Give the extent of all uninfected red blood cells.
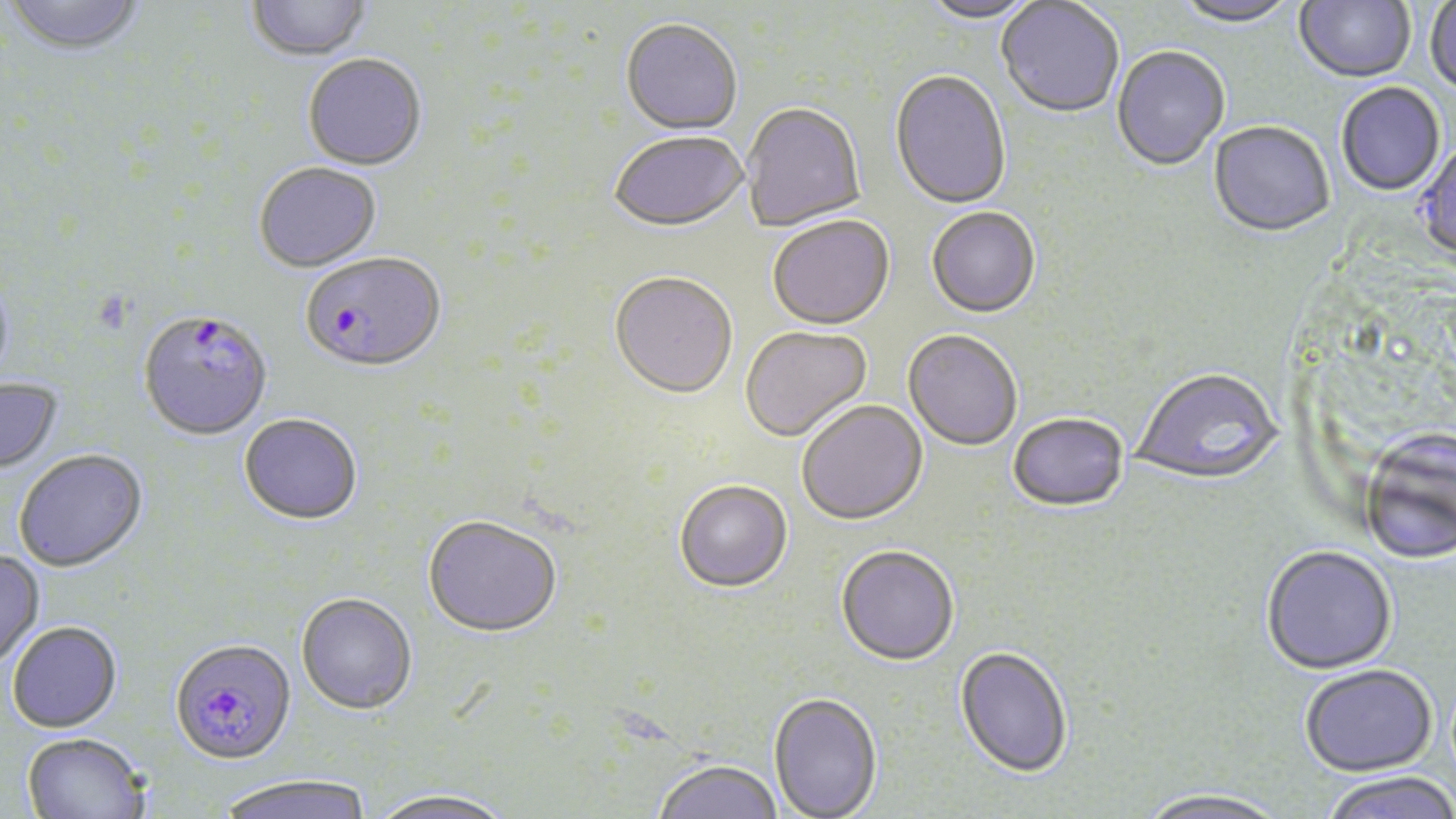

Approximate bounding boxes as named x1/y1/x2/y2 corners in pixels.
Uninfected red blood cells: (x1=4, y1=0, x2=147, y2=59), (x1=920, y1=0, x2=1041, y2=27), (x1=1294, y1=0, x2=1416, y2=85), (x1=245, y1=1, x2=374, y2=64), (x1=996, y1=1, x2=1124, y2=120), (x1=1172, y1=1, x2=1299, y2=29), (x1=1425, y1=1, x2=1456, y2=97), (x1=620, y1=21, x2=742, y2=137), (x1=1112, y1=47, x2=1230, y2=173), (x1=303, y1=56, x2=427, y2=173), (x1=889, y1=72, x2=1011, y2=211), (x1=1336, y1=84, x2=1445, y2=197), (x1=741, y1=105, x2=866, y2=232), (x1=1208, y1=123, x2=1335, y2=239), (x1=610, y1=134, x2=748, y2=234), (x1=1414, y1=142, x2=1456, y2=264), (x1=254, y1=164, x2=382, y2=274), (x1=926, y1=209, x2=1041, y2=321), (x1=768, y1=218, x2=895, y2=332), (x1=0, y1=274, x2=15, y2=389), (x1=609, y1=275, x2=738, y2=402), (x1=740, y1=327, x2=873, y2=444), (x1=903, y1=332, x2=1022, y2=452), (x1=1133, y1=370, x2=1284, y2=487), (x1=0, y1=379, x2=64, y2=478), (x1=797, y1=402, x2=928, y2=528), (x1=239, y1=416, x2=362, y2=528), (x1=1008, y1=416, x2=1128, y2=514), (x1=1360, y1=431, x2=1456, y2=565), (x1=14, y1=451, x2=148, y2=573), (x1=674, y1=482, x2=793, y2=595), (x1=422, y1=518, x2=562, y2=641), (x1=1260, y1=546, x2=1397, y2=676), (x1=836, y1=547, x2=959, y2=669), (x1=0, y1=551, x2=45, y2=669), (x1=296, y1=595, x2=418, y2=718), (x1=7, y1=623, x2=123, y2=734), (x1=954, y1=648, x2=1073, y2=780), (x1=1300, y1=664, x2=1438, y2=776), (x1=768, y1=694, x2=882, y2=819), (x1=22, y1=734, x2=151, y2=819), (x1=652, y1=761, x2=784, y2=819), (x1=1318, y1=772, x2=1456, y2=819), (x1=215, y1=778, x2=373, y2=819), (x1=1135, y1=789, x2=1290, y2=819), (x1=366, y1=790, x2=515, y2=819).

slide_level_diagnosis: Plasmodium falciparum
modality: light microscopy
stain: May-Grünwald-Giemsa
field_of_view: single
preparation: thin blood smear
image_size: 1456×819 pixels
plasmodium_falciparum_infected_red_blood_cell_locations: 'approximate bounding boxes as named x1/y1/x2/y2 corners in pixels: (x1=299, y1=254, x2=446, y2=375), (x1=138, y1=312, x2=273, y2=443), (x1=170, y1=641, x2=296, y2=768)'
magnification: 1000x